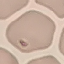
Summary:
  - Malaria status: uninfected
  - Stain: Giemsa
  - Capture: smartphone camera at the microscope eyepiece
  - Preparation: thin blood film
  - Image type: automatically extracted cell patch, resized to 64 × 64 pixels